Identify the parasite.
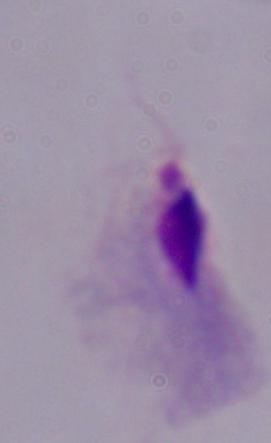

A trichomonad.

Micrograph. 1000x magnification.